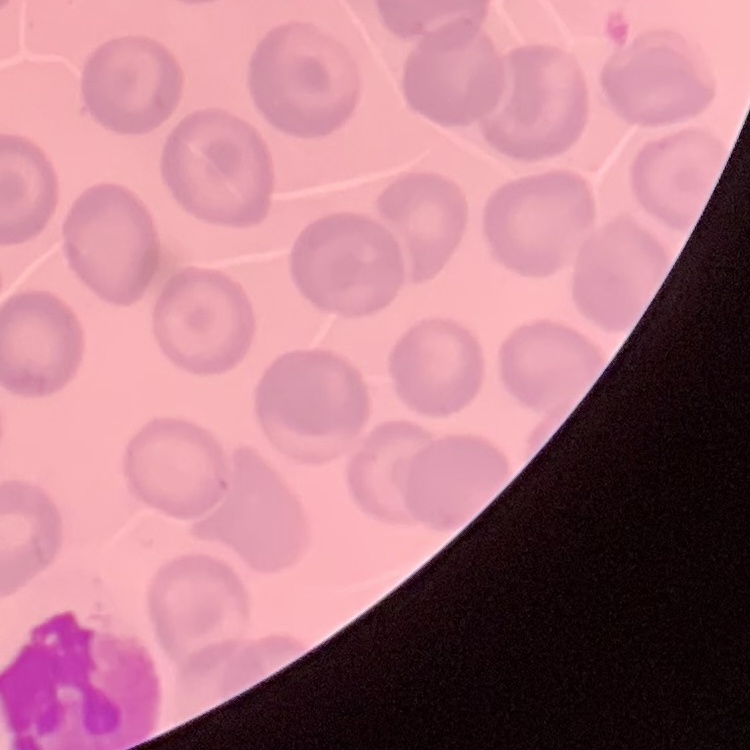

Summary:
  - Red blood cell morphology: no rouleaux formation
  - Preparation: thin blood smear
  - Image type: one tile cut from a larger photomicrograph
  - Stain: Field's or Giemsa